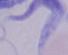

Captured at 1000x magnification. A trypanosome is shown. Micrograph.